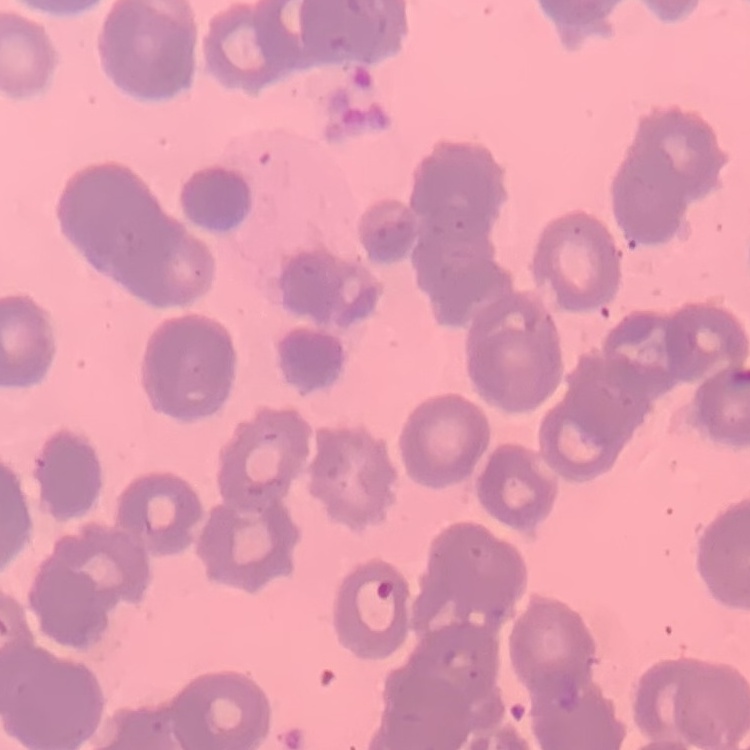

red blood cell morphology = rouleaux formation
image type = one tile cut from a larger photomicrograph
stain = Field's or Giemsa
preparation = thin peripheral smear